Comment on the morphology of the erythrocytes.
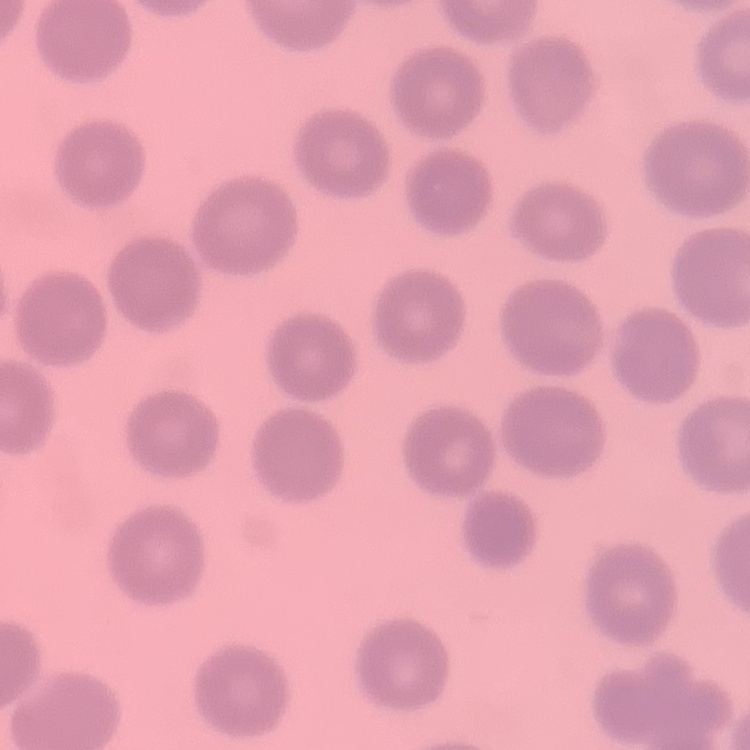

No rouleaux formation.

preparation = thin blood film
stain = Field's or Giemsa
image type = square crop of a larger photomicrograph